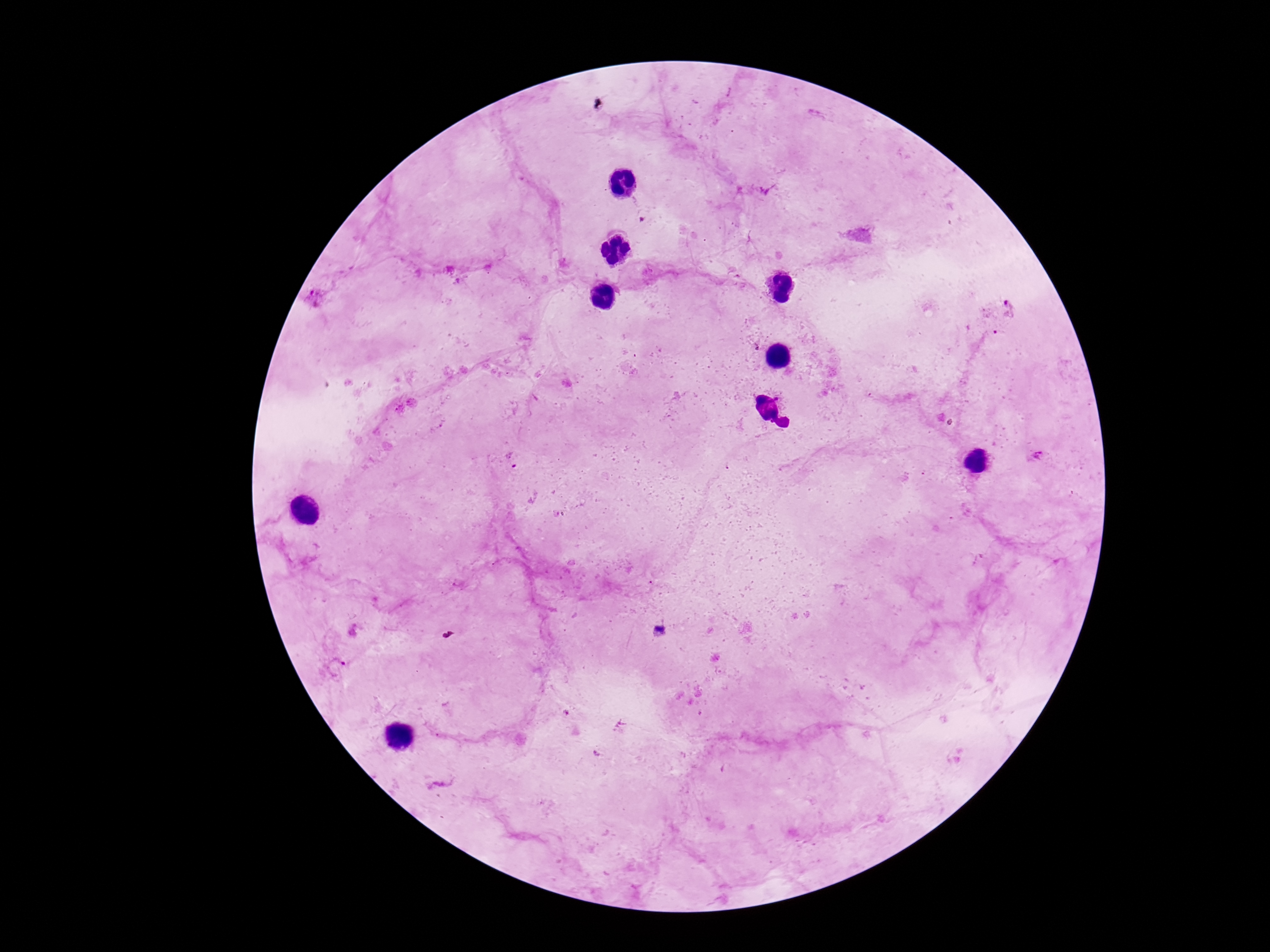

Approximate object centers, in pixels from the top-left corner. Plasmodium parasite locations: (x=318, y=300), (x=1035, y=457), (x=511, y=459), (x=657, y=631), (x=335, y=666). Image is 1270×952 pixels. Smartphone photograph taken through the microscope eyepiece. 100x magnification. Patient malaria status: infected. Giemsa-stained preparation. Thick blood smear. One field from this slide.